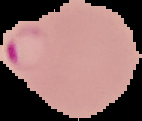

Summary:
  - Preparation: thin blood film
  - Image type: cell region segmented out of the field of view; surrounding area masked to black
  - Malaria status: parasitized
  - Image size: 142×121 pixels